Classify this cell by malaria status.
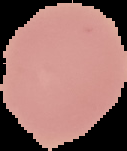
It is uninfected.

Summary:
  - Preparation: thin blood smear
  - Image type: segmented cell region with the area outside set to black
  - Image size: 127×151 pixels